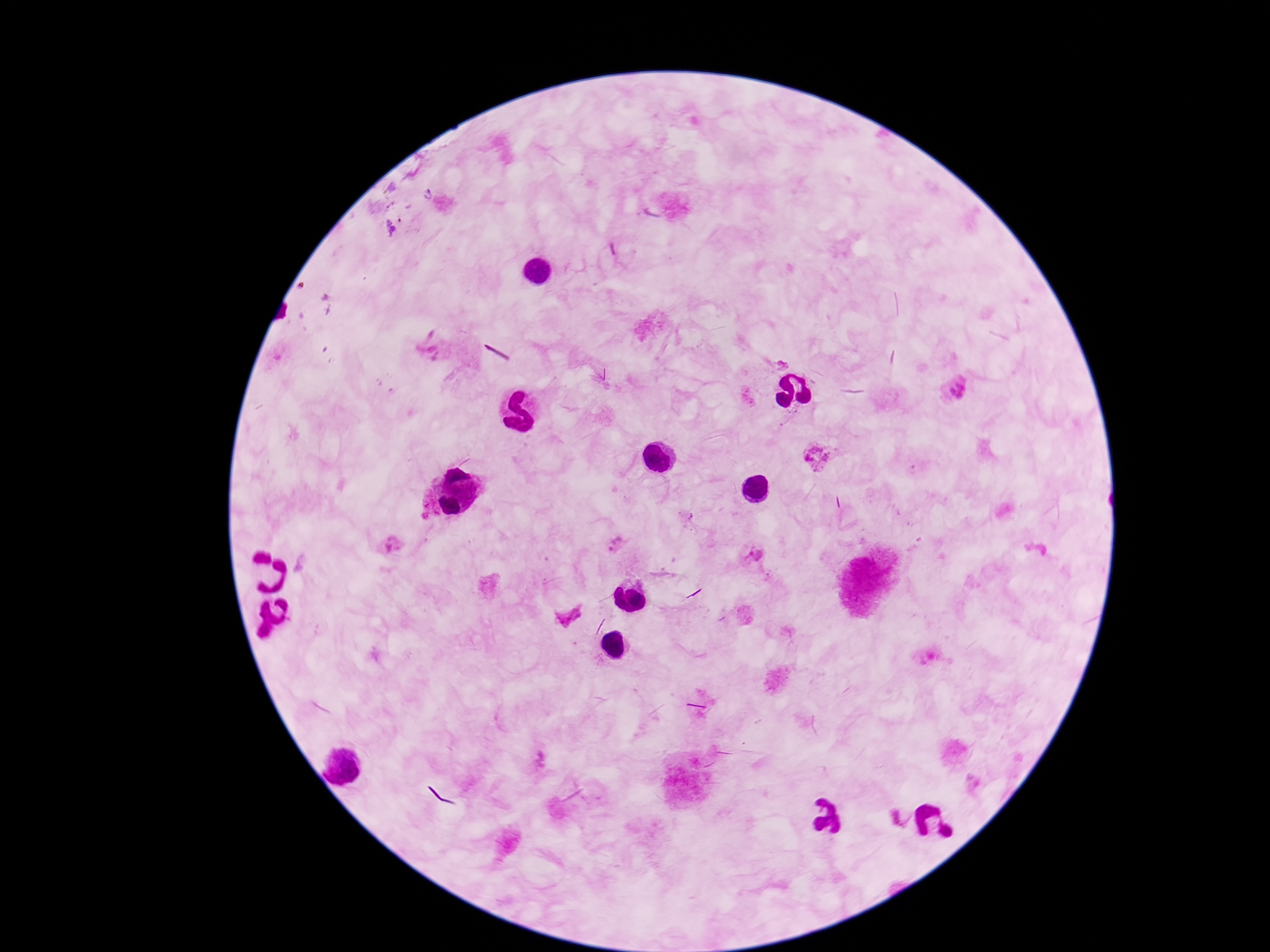

Approximate centers as [x, y] in pixels.
Summary:
  - Plasmodium parasite locations: [426, 193], [389, 228], [434, 348], [954, 394], [818, 455], [617, 543], [391, 546], [754, 554], [567, 616], [540, 757], [900, 819]
  - Preparation: thick blood smear
  - Field of view: single
  - Capture: smartphone camera through the microscope eyepiece
  - Stain: Giemsa
  - Image size: 1270×952 pixels
  - Patient malaria status: infected
  - Magnification: 100x